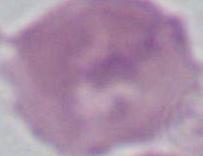

modality = photomicrograph
magnification = 1000x
identification = red blood cell